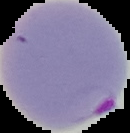
result = Plasmodium parasites detected
preparation = thin blood smear
image size = 130×133 pixels
image type = cell region segmented out of the field of view; surrounding area masked to black